Give the preparation type.
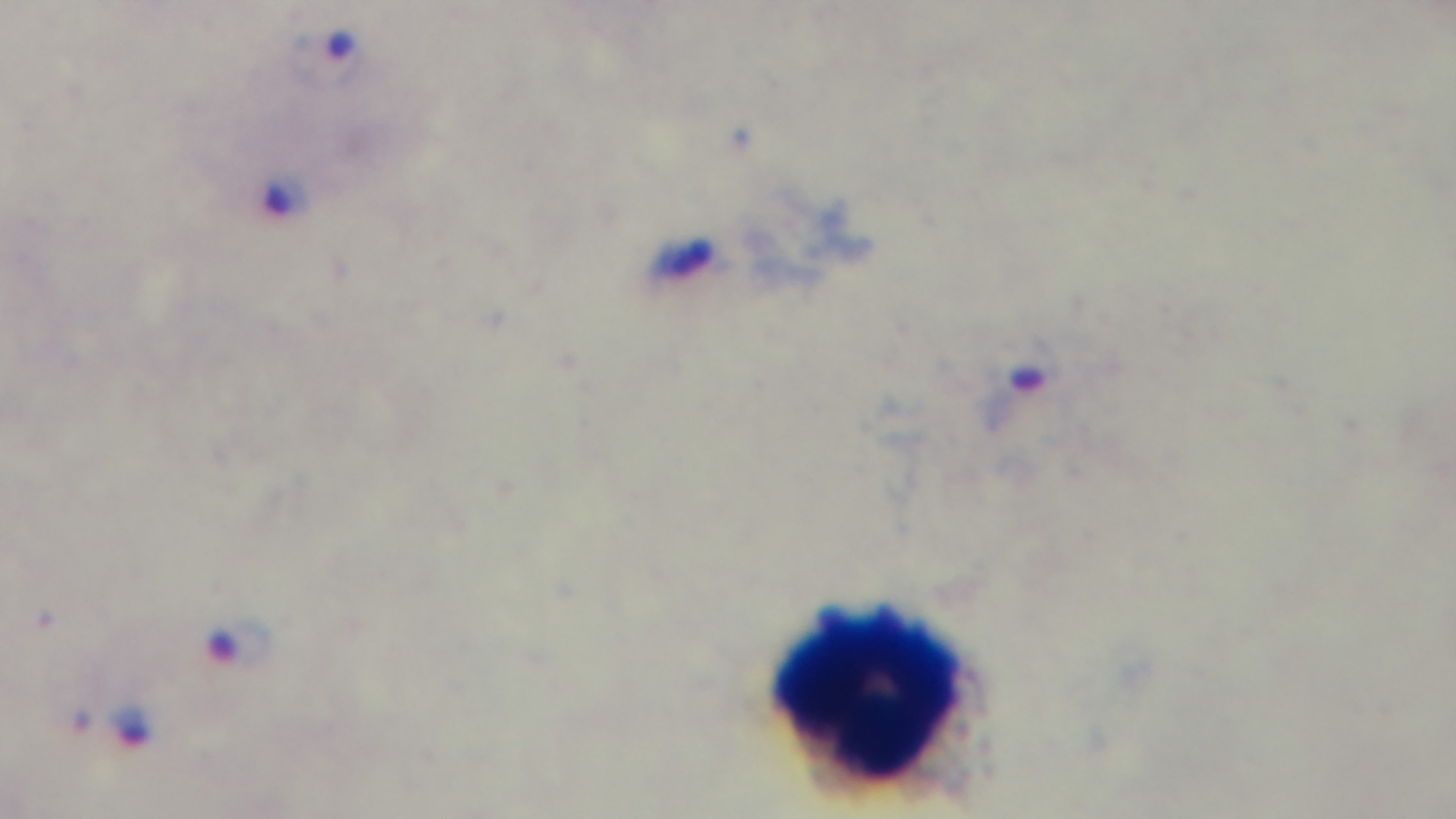

It is a thick blood film.

Light microscopy. Malaria status: positive. Mounted 4K digital camera. Giemsa stain. One field from the slide. 100x oil-immersion objective.